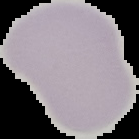
Summary:
  - Preparation: thin blood smear
  - Image size: 139×139 pixels
  - Image type: cell region segmented out of the field of view; surrounding area masked to black
  - Malaria status: uninfected